State which cell type is depicted.
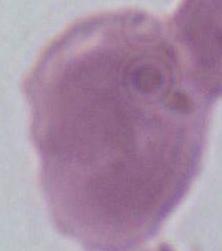

This is an erythrocyte.

Summary:
  - Modality: micrograph
  - Magnification: 1000x